Identify the parasite.
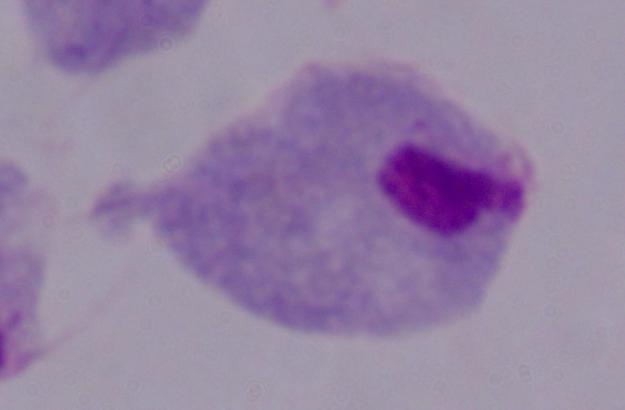
A trichomonad.

{
  "modality": "photomicrograph",
  "magnification": "1000x"
}